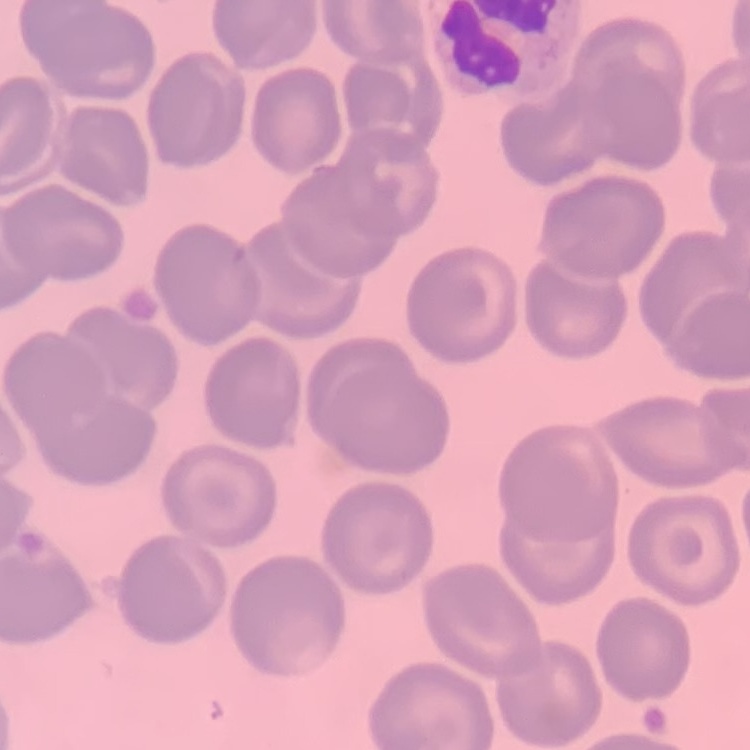

erythrocyte morphology = no rouleaux formation
stain = Field's or Giemsa
preparation = thin blood smear
image type = one tile cut from a larger photomicrograph